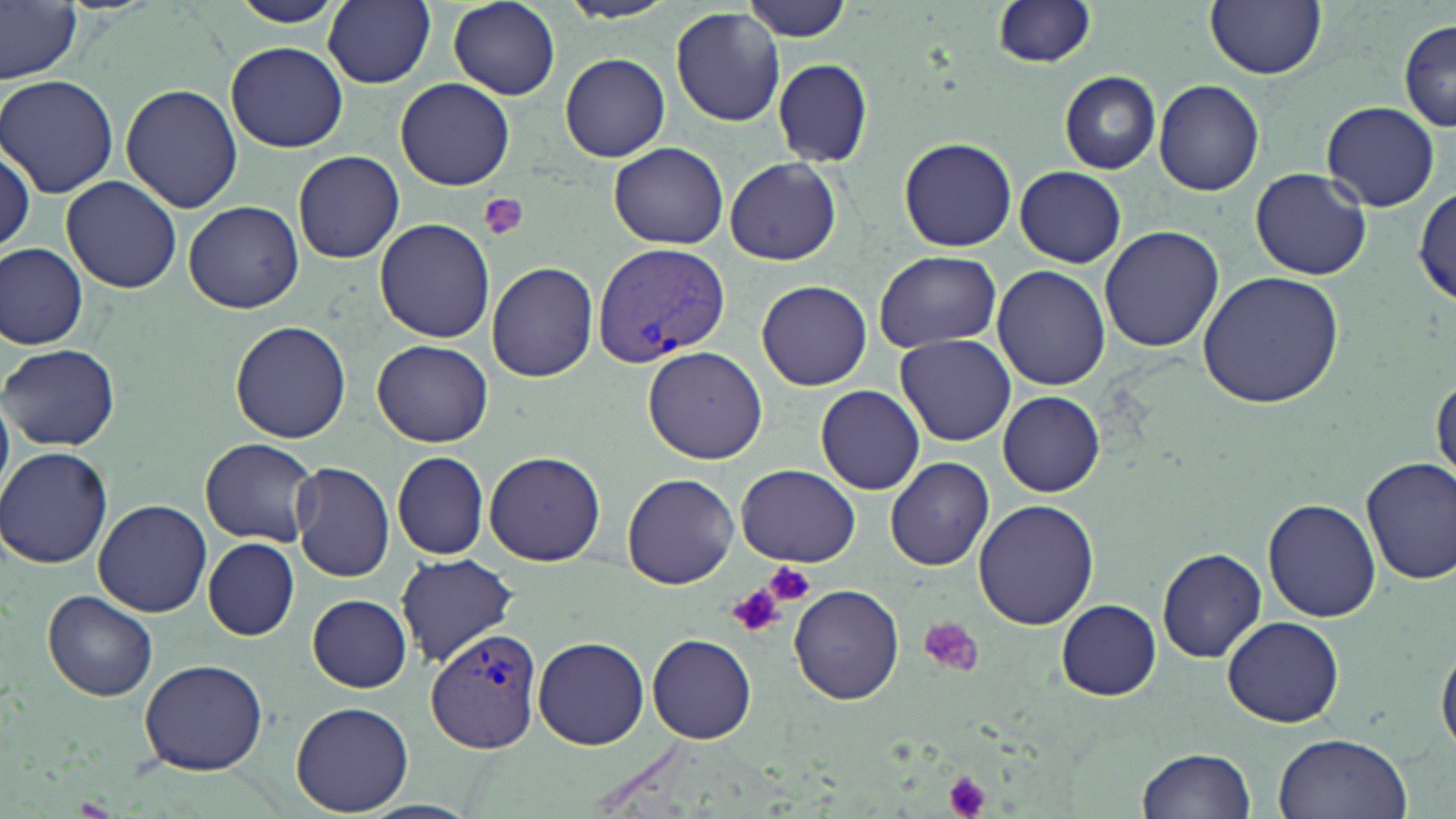
slide-level diagnosis = Plasmodium vivax
magnification = 1000x
image size = 1456×819 pixels
preparation = thin blood film
modality = optical microscopy
stain = May-Grünwald-Giemsa
Plasmodium vivax-infected red blood cell locations = approximate bounding boxes as [x1, y1, x2, y2] in pixels: [592, 240, 731, 364], [425, 627, 542, 752]
uninfected red blood cell locations = approximate bounding boxes as [x1, y1, x2, y2] in pixels: [227, 0, 343, 27], [324, 0, 436, 88], [740, 0, 855, 42], [992, 0, 1099, 69], [0, 1, 81, 84], [554, 1, 678, 24], [1206, 1, 1326, 80], [445, 2, 562, 99], [671, 8, 787, 127], [1397, 20, 1456, 133], [226, 40, 348, 153], [560, 53, 670, 161], [772, 58, 873, 167], [1059, 71, 1160, 174], [1, 74, 120, 197], [396, 77, 515, 190], [1153, 79, 1264, 197], [120, 83, 245, 215], [1319, 101, 1443, 211], [898, 136, 1017, 251], [608, 143, 728, 249], [0, 146, 34, 255], [294, 149, 405, 263], [724, 157, 842, 266], [1013, 165, 1126, 267], [1249, 167, 1371, 280], [61, 175, 183, 293], [1413, 184, 1455, 305], [183, 201, 304, 312], [374, 217, 495, 343], [1098, 224, 1225, 354], [0, 244, 88, 348], [873, 250, 1002, 352], [488, 262, 597, 382], [992, 265, 1110, 390], [1195, 270, 1345, 410], [757, 279, 872, 389], [230, 320, 352, 443], [896, 334, 1017, 446], [373, 340, 493, 448], [2, 343, 119, 452], [643, 346, 769, 466], [1432, 374, 1455, 487], [814, 385, 924, 495], [997, 391, 1103, 496], [200, 437, 320, 547], [0, 447, 116, 569], [393, 451, 489, 561], [483, 451, 605, 566], [1361, 455, 1456, 586], [886, 456, 994, 571], [290, 461, 395, 582], [735, 464, 860, 567], [623, 472, 739, 589], [972, 498, 1096, 630], [93, 499, 213, 618], [1262, 499, 1381, 622], [203, 538, 299, 640], [1157, 547, 1265, 663], [396, 553, 519, 667], [789, 582, 904, 705], [44, 591, 158, 702], [308, 594, 410, 691], [1057, 600, 1161, 699], [1221, 616, 1346, 728], [648, 633, 757, 743], [1436, 634, 1456, 761], [532, 636, 649, 750], [139, 658, 268, 775], [291, 702, 415, 815], [1273, 731, 1413, 819], [1139, 746, 1256, 818]
field of view = one of a larger specimen
platelet locations = approximate bounding boxes as [x1, y1, x2, y2] in pixels: [480, 193, 530, 241], [764, 561, 815, 606], [726, 584, 785, 638], [915, 617, 986, 679], [940, 769, 993, 819]